State the blood parasite species.
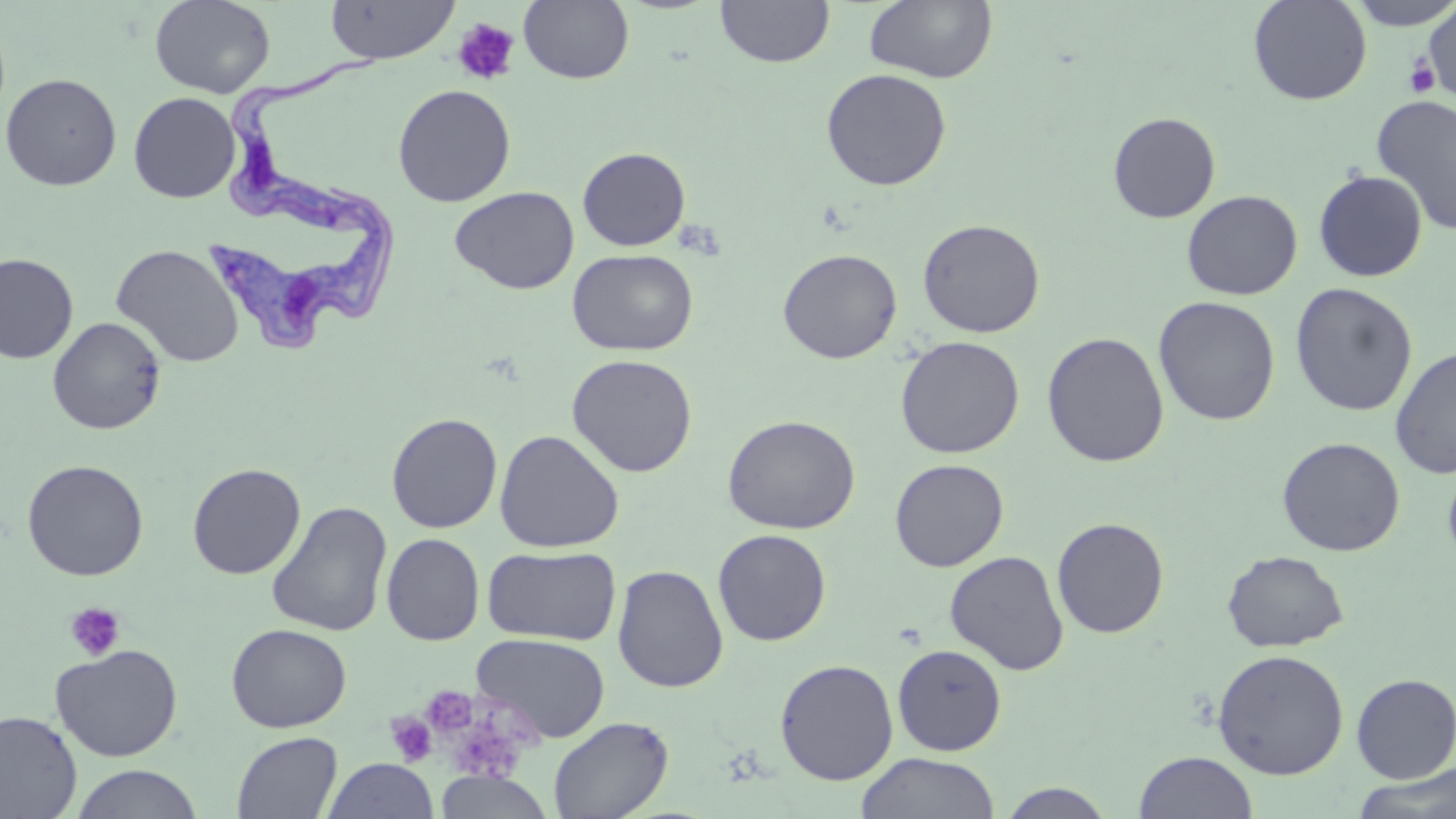
Trypanosoma brucei.

Summary:
  - Coordinate format: approximate bounding boxes as (x1,y1)-(x2,y2) corner pairs in pixels
  - Platelet locations: (452,17)-(520,86), (1404,56)-(1441,99), (675,219)-(725,261), (64,601)-(126,662), (421,685)-(477,737), (385,711)-(437,766)
  - Uninfected red blood cell locations: (149,0)-(276,98), (325,0)-(459,64), (519,0)-(634,84), (715,0)-(835,68), (863,0)-(998,84), (1248,0)-(1372,106), (1345,0)-(1456,30), (1422,3)-(1456,103), (820,68)-(952,191), (1,72)-(122,191), (392,84)-(516,207), (128,92)-(240,203), (1372,95)-(1456,236), (1107,112)-(1221,223), (577,146)-(690,251), (1313,170)-(1428,282), (449,186)-(579,294), (1181,190)-(1303,300), (917,218)-(1045,338), (110,243)-(244,367), (777,248)-(902,364), (567,249)-(698,356), (0,253)-(78,364), (1290,283)-(1418,417), (1153,295)-(1281,426), (48,316)-(166,435), (1042,331)-(1169,467), (895,335)-(1025,459), (1389,345)-(1456,479), (566,353)-(698,477), (386,412)-(503,533), (722,414)-(860,534), (494,429)-(624,553), (1276,437)-(1406,556), (1442,456)-(1456,571), (889,458)-(1008,571), (22,459)-(149,581), (187,463)-(306,579), (266,501)-(393,637), (1052,516)-(1169,638), (712,529)-(831,646), (381,533)-(485,646), (482,545)-(621,646), (1221,549)-(1349,653), (945,550)-(1069,675), (613,564)-(729,693), (226,623)-(351,733), (472,632)-(610,742), (51,643)-(183,761), (892,643)-(1007,755), (1212,649)-(1349,780), (774,658)-(899,785), (1351,673)-(1456,782), (0,709)-(83,819), (547,716)-(673,819), (231,731)-(343,818), (1133,750)-(1258,819), (855,752)-(1000,819), (322,758)-(438,819), (69,764)-(205,819), (1349,765)-(1456,819), (433,771)-(554,818), (996,783)-(1117,818)
  - Trypanosoma brucei locations: (218,43)-(397,242), (205,186)-(406,357)
  - Field of view: single
  - Magnification: 1000x
  - Preparation: thin blood smear
  - Stain: May-Grünwald-Giemsa
  - Image size: 1456×819 pixels
  - Modality: light microscopy